Assess this cell for malaria.
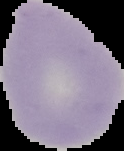

Uninfected.

The area outside the segmented cell region is set to black. From a thin blood film. Image is 124×151 pixels.